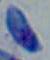 Toxoplasma gondii is seen. Captured at 1000x magnification. Micrograph.